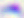
Photomicrograph. Toxoplasma gondii is seen. 400x magnification.